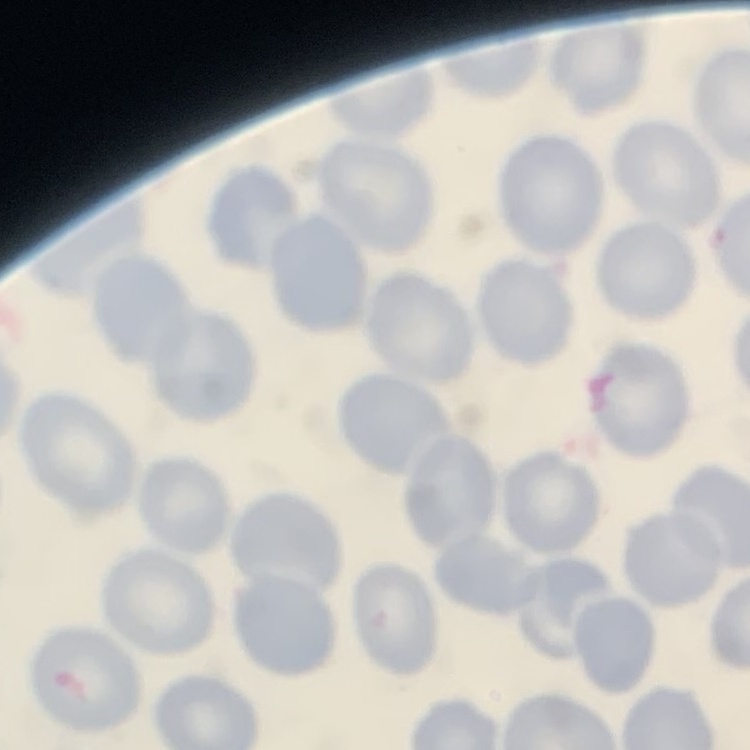 The red blood cells show no rouleaux formation. Stained with either Field's or Giemsa. One tile cut from a larger photomicrograph. Thin peripheral smear.